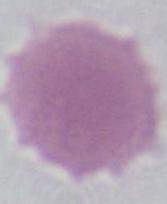
Summary:
  - Modality: photomicrograph
  - Identification: red blood cell
  - Magnification: 1000x